Identify the cell.
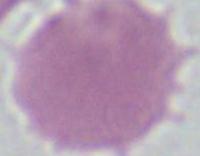

This is an erythrocyte.

Summary:
  - Magnification: 1000x
  - Modality: photomicrograph